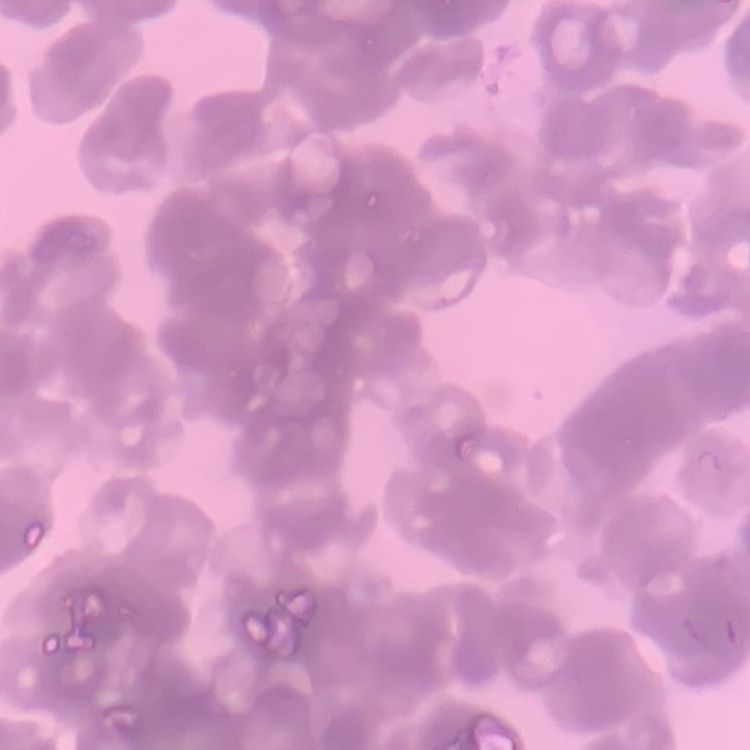 The red blood cells exhibit rouleaux formation. Thin blood film. Stained with either Field's or Giemsa. One tile cut from a larger photomicrograph.